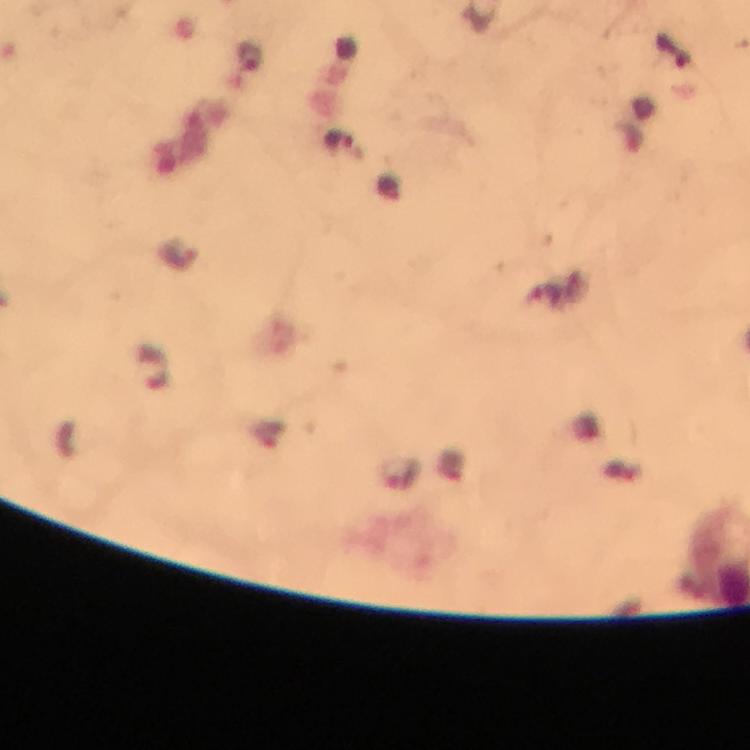
Approximate centers as [x, y] in pixels. Malaria parasite locations: [339, 143], [400, 472]. Photographed through the microscope with a smartphone camera. Giemsa-stained preparation. Immersion oil was used. Image is 750×750 pixels. Thick blood smear. From a diagnostic examination for malaria. At 100x magnification. A crop from one field of view.